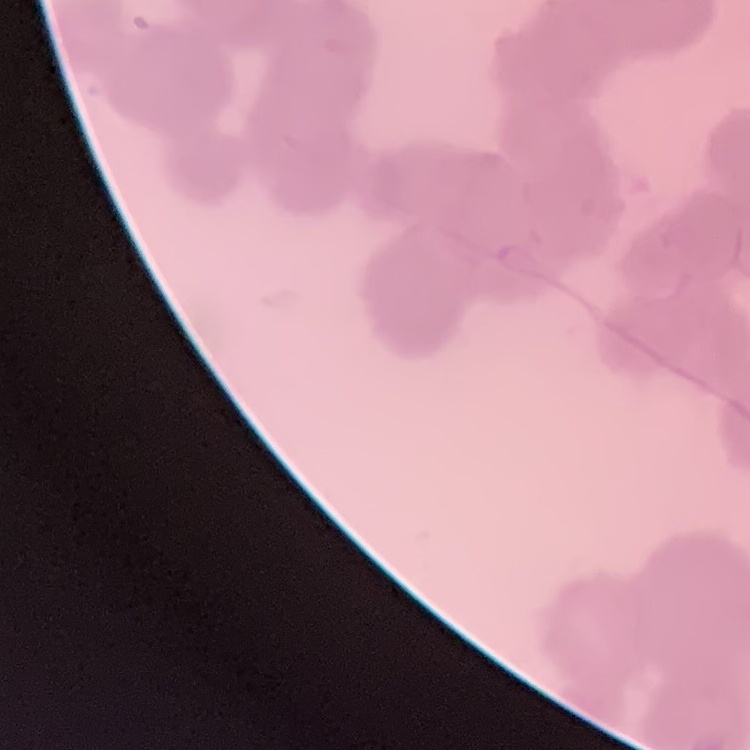
erythrocyte morphology = rouleaux formation
preparation = thin peripheral smear
stain = Field's or Giemsa
image type = square crop of a larger photomicrograph